Outline each blood parasite and name the species.
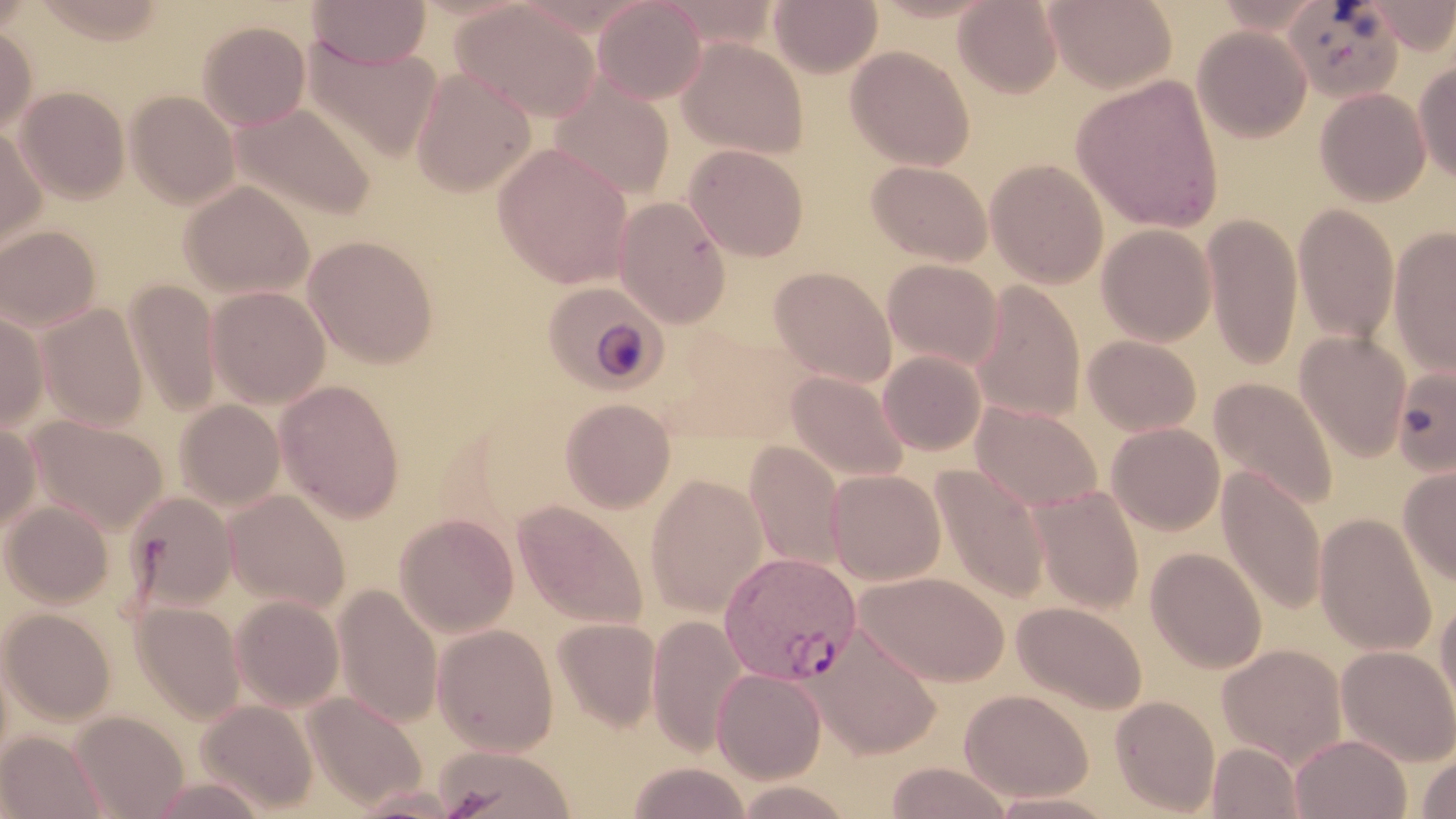
Approximate bounding boxes as (x1,y1)-(x2,y2) corner pairs in pixels.
Plasmodium vivax-infected red blood cells: (718,551)-(862,684).
No Plasmodium falciparum, Plasmodium ovale, Plasmodium malariae, Babesia divergens, or Trypanosoma brucei observed.

Summary:
  - Uninfected red blood cell locations: (29,0)-(167,43), (307,0)-(432,69), (655,0)-(781,51), (768,0)-(882,77), (954,0)-(1063,98), (1045,0)-(1177,93), (1365,0)-(1455,54), (593,1)-(707,104), (1283,1)-(1405,102), (451,3)-(600,121), (196,20)-(311,131), (0,25)-(37,135), (1192,25)-(1312,143), (303,37)-(442,162), (677,37)-(810,160), (845,45)-(975,171), (1414,60)-(1456,184), (410,69)-(535,197), (1072,75)-(1224,233), (548,76)-(675,200), (15,86)-(130,204), (1315,88)-(1431,206), (126,90)-(240,209), (231,102)-(377,223), (0,127)-(47,259), (493,144)-(634,289), (684,144)-(809,261), (985,158)-(1109,288), (866,160)-(993,266), (179,180)-(314,299), (612,196)-(731,328), (1292,203)-(1399,345), (1201,213)-(1303,370), (0,224)-(101,331), (1097,224)-(1217,346), (1388,227)-(1456,377), (303,236)-(439,369), (882,259)-(1003,370), (769,266)-(896,386), (125,280)-(222,418), (543,281)-(669,395), (970,281)-(1086,422), (206,286)-(330,408), (38,303)-(148,429), (0,308)-(50,431), (1295,331)-(1412,462), (1083,334)-(1201,436), (878,350)-(986,455), (1392,364)-(1456,476), (785,371)-(909,484), (1209,377)-(1338,511), (275,379)-(406,522), (560,398)-(675,513), (175,400)-(285,510), (970,400)-(1104,512), (26,415)-(168,533), (0,419)-(41,533), (1107,422)-(1225,535), (744,441)-(846,571), (1398,462)-(1456,586), (931,466)-(1051,604), (1217,466)-(1327,616), (826,469)-(946,585), (646,473)-(767,617), (1031,487)-(1144,614), (224,490)-(350,613), (124,491)-(236,611), (2,500)-(113,608), (513,500)-(649,631), (1315,513)-(1437,657), (395,514)-(518,636), (1145,547)-(1267,674), (855,571)-(1010,686), (333,584)-(443,728), (1434,593)-(1456,726), (231,595)-(344,711), (1012,601)-(1147,715), (132,602)-(245,724), (1,608)-(116,725), (647,615)-(748,756), (553,617)-(662,732), (432,624)-(559,756), (816,626)-(941,758), (1217,644)-(1348,768), (1336,645)-(1456,766), (712,668)-(826,783), (960,689)-(1094,801), (304,692)-(427,811), (1111,695)-(1220,816), (196,699)-(317,814), (69,711)-(189,819), (1,731)-(108,819), (1290,733)-(1411,819), (1207,742)-(1303,818), (433,745)-(577,819), (1417,752)-(1456,818), (884,761)-(1015,819), (625,762)-(752,819), (148,775)-(270,818), (989,791)-(1119,818)
  - Slide-level diagnosis: Plasmodium vivax
  - Field of view: single
  - Modality: optical microscopy
  - Magnification: 1000x
  - Stain: May-Grünwald-Giemsa
  - Image size: 1456×819 pixels
  - Preparation: thin blood smear